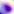
Toxoplasma gondii is shown. Photomicrograph. Captured at 400x magnification.